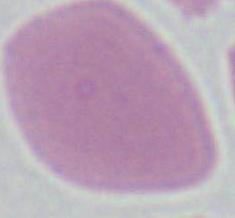
Photomicrograph. Captured at 1000x magnification. A red blood cell is shown.